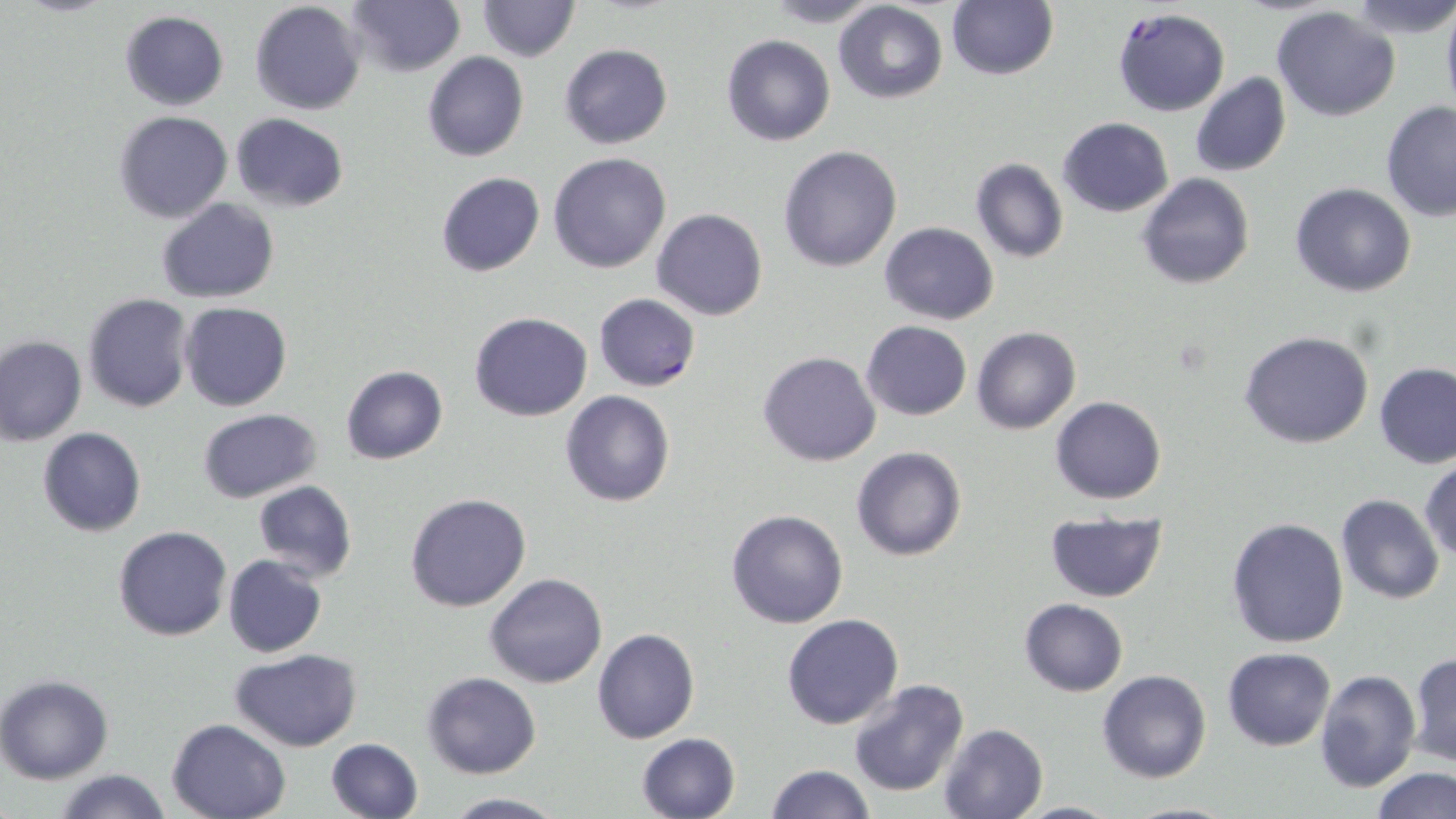
Plasmodium falciparum-infected red blood cell locations = approximate bounding boxes as (x1,y1)-(x2,y2) corner pairs in pixels: (1112,8)-(1231,116), (593,293)-(701,391)
slide-level diagnosis = Plasmodium falciparum
image size = 1456×819 pixels
field of view = single
uninfected red blood cell locations = approximate bounding boxes as (x1,y1)-(x2,y2) corner pairs in pixels: (476,0)-(579,60), (1348,0)-(1456,39), (1440,0)-(1456,122), (249,1)-(367,116), (347,1)-(464,77), (758,1)-(889,27), (834,1)-(947,103), (945,1)-(1059,81), (1271,6)-(1401,121), (119,11)-(230,111), (721,34)-(835,146), (558,43)-(672,149), (423,52)-(529,161), (1190,73)-(1291,177), (1380,101)-(1456,223), (114,110)-(233,222), (230,113)-(350,212), (1059,117)-(1174,218), (777,145)-(903,272), (549,153)-(673,274), (970,158)-(1068,264), (434,172)-(546,277), (1138,174)-(1254,291), (1290,183)-(1417,297), (157,198)-(278,303), (651,208)-(767,320), (879,222)-(999,325), (82,293)-(194,412), (180,301)-(292,412), (469,312)-(593,422), (862,321)-(970,420), (972,325)-(1080,435), (1240,330)-(1374,448), (0,334)-(87,446), (757,351)-(881,466), (1374,362)-(1455,468), (341,365)-(448,465), (559,390)-(676,508), (1051,396)-(1167,504), (196,408)-(323,503), (36,427)-(146,537), (851,446)-(966,562), (1419,461)-(1456,563), (252,480)-(357,583), (404,492)-(531,612), (1336,493)-(1444,604), (726,508)-(849,629), (1044,512)-(1168,600), (1226,517)-(1348,649), (112,525)-(232,642), (223,555)-(328,657), (483,573)-(609,688), (1019,597)-(1128,696), (781,613)-(904,731), (592,628)-(700,744), (1223,647)-(1335,750), (229,648)-(362,752), (1408,653)-(1455,765), (1314,668)-(1421,794), (1097,669)-(1212,784), (423,672)-(541,778), (0,676)-(115,783), (847,680)-(971,797), (165,718)-(292,819), (938,722)-(1051,818), (637,734)-(740,819), (325,738)-(424,819), (764,764)-(873,819), (1371,767)-(1456,819), (55,769)-(173,819), (439,793)-(568,818), (1009,799)-(1123,817), (1115,799)-(1244,818)
magnification = 1000x
preparation = thin blood smear
modality = optical microscopy
stain = May-Grünwald-Giemsa